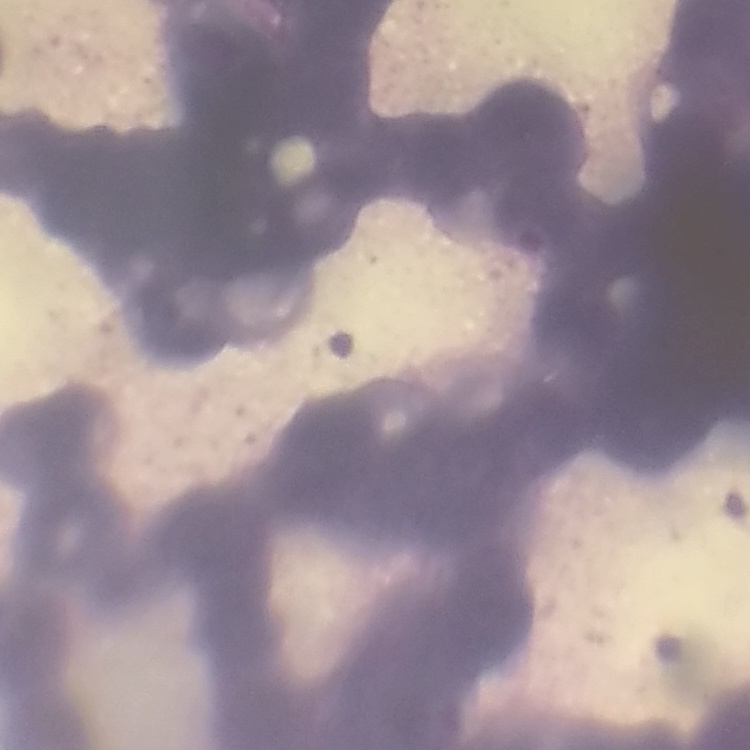 The erythrocytes exhibit rouleaux formation. Stained with either Field's or Giemsa. Thin blood smear. Square crop of a larger photomicrograph.